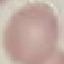
Summary:
  - Result: no malaria parasites detected
  - Capture: smartphone through the microscope eyepiece
  - Stain: Giemsa
  - Preparation: thin blood smear
  - Image type: cell patch, automatically extracted from a larger field of view and resized to 64 × 64 pixels